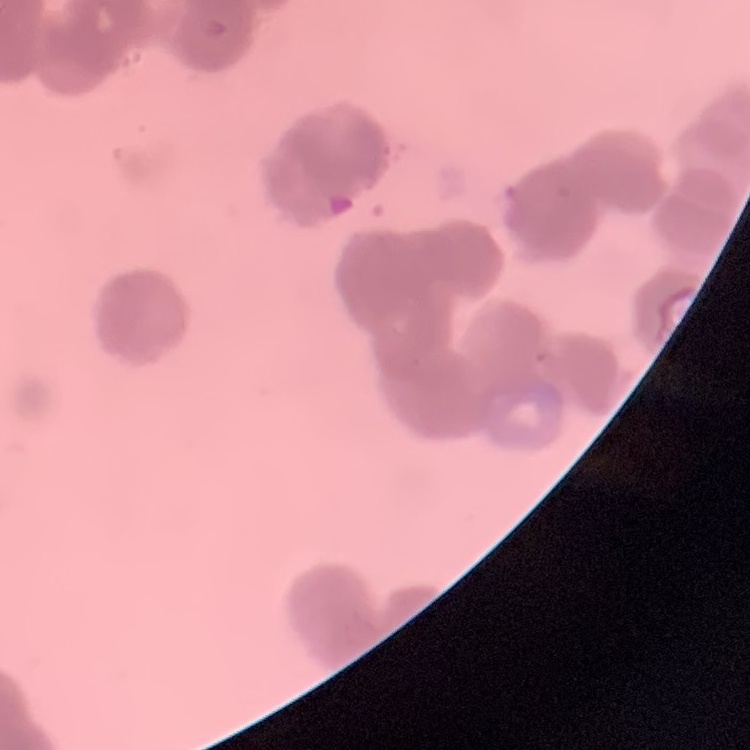 The erythrocytes show rouleaux formation. Square crop of a larger photomicrograph. Field's or Giemsa stain. Thin peripheral smear.